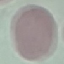

Malaria status: uninfected. Thin smear of blood. Giemsa-stained preparation. Automatically extracted cell patch, resized to 64 × 64 pixels. Photographed with a smartphone camera at the microscope eyepiece.